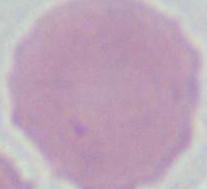

Summary:
  - Magnification: 1000x
  - Modality: micrograph
  - Identification: erythrocyte